Outline each blood parasite and name the species.
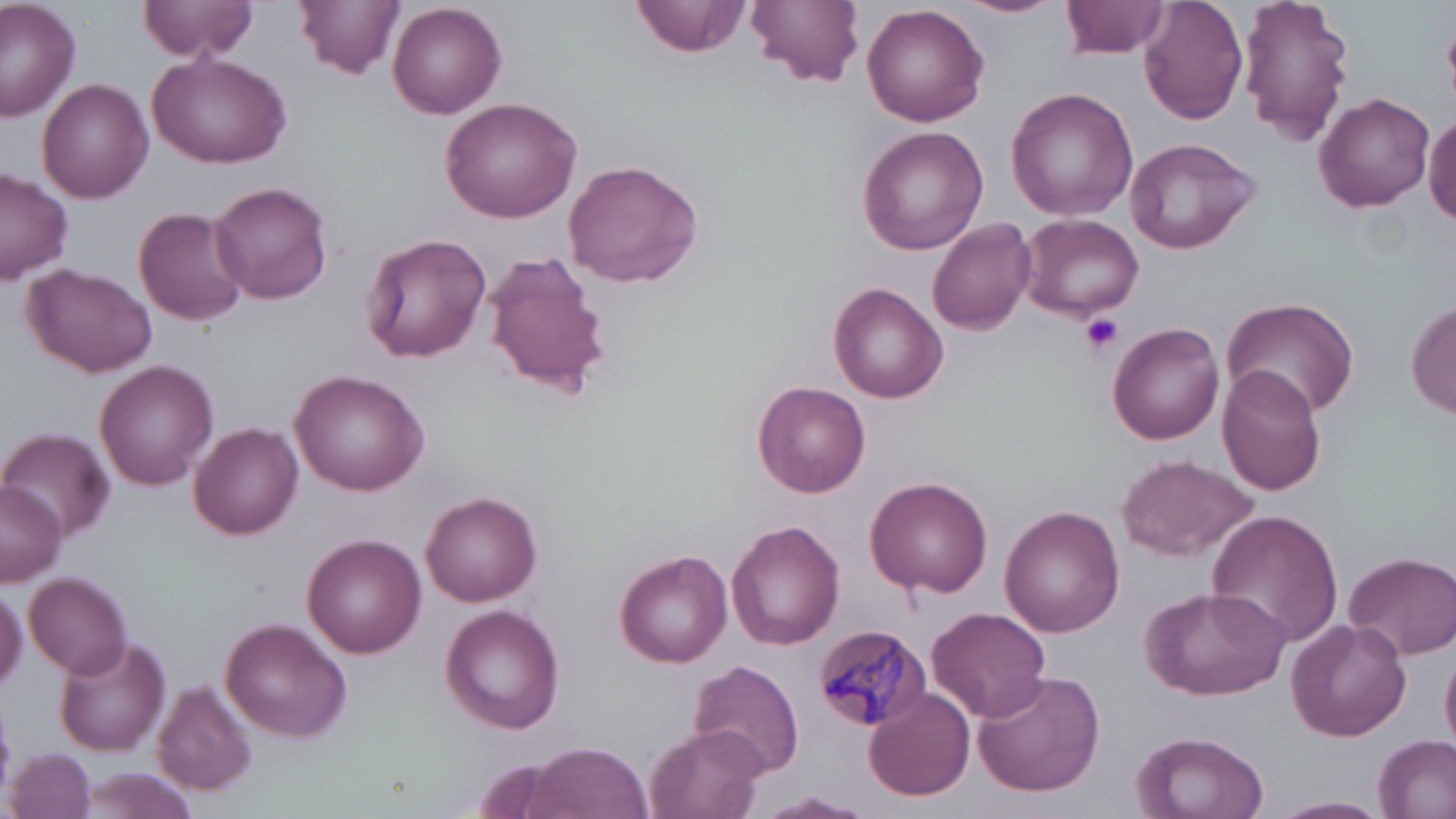

Approximate bounding boxes as (x1,y1)-(x2,y2) corner pairs in pixels.
Plasmodium malariae-infected red blood cells: (810,625)-(930,732).
No Plasmodium falciparum, Plasmodium ovale, Plasmodium vivax, Babesia divergens, or Trypanosoma brucei observed.

Summary:
  - Platelet locations: (1081,315)-(1124,355)
  - Uninfected red blood cell locations: (0,0)-(81,120), (139,0)-(260,61), (298,0)-(403,78), (632,0)-(753,57), (748,0)-(864,89), (955,0)-(1065,19), (1061,0)-(1171,59), (1138,0)-(1249,125), (1239,0)-(1355,146), (388,1)-(506,119), (861,4)-(991,128), (146,51)-(294,168), (37,78)-(154,204), (1006,86)-(1138,221), (1314,91)-(1435,211), (439,95)-(585,222), (1424,108)-(1456,226), (856,125)-(989,256), (1123,136)-(1260,254), (563,159)-(703,287), (0,168)-(74,285), (211,181)-(332,305), (132,205)-(249,326), (1017,213)-(1144,322), (928,218)-(1037,335), (361,231)-(495,364), (481,250)-(612,398), (23,263)-(156,377), (828,281)-(947,404), (1222,295)-(1360,416), (1408,298)-(1456,423), (1108,321)-(1225,445), (95,360)-(218,489), (1216,365)-(1327,496), (291,369)-(429,496), (753,379)-(870,496), (191,421)-(304,541), (4,430)-(115,539), (1116,454)-(1260,561), (865,476)-(993,598), (0,480)-(68,584), (420,491)-(542,607), (1000,505)-(1125,635), (1207,509)-(1345,650), (729,519)-(847,651), (303,532)-(426,656), (1344,549)-(1456,660), (615,550)-(732,667), (1312,568)-(1428,709), (25,572)-(133,678), (0,583)-(27,697), (1139,585)-(1292,702), (441,603)-(566,735), (926,606)-(1054,722), (219,616)-(352,742), (1285,617)-(1412,742), (53,637)-(172,758), (1441,645)-(1456,758), (689,659)-(806,778), (970,670)-(1106,797), (154,678)-(257,798), (863,687)-(976,802), (645,725)-(768,819), (1129,731)-(1271,819), (1373,735)-(1456,819), (523,741)-(653,819), (7,748)-(97,819), (69,765)-(205,819), (754,792)-(876,818), (1267,795)-(1391,819)
  - Slide-level diagnosis: Plasmodium malariae
  - Image size: 1456×819 pixels
  - Field of view: one of a larger specimen
  - Stain: May-Grünwald-Giemsa
  - Magnification: 1000x
  - Modality: optical microscopy
  - Preparation: thin blood smear